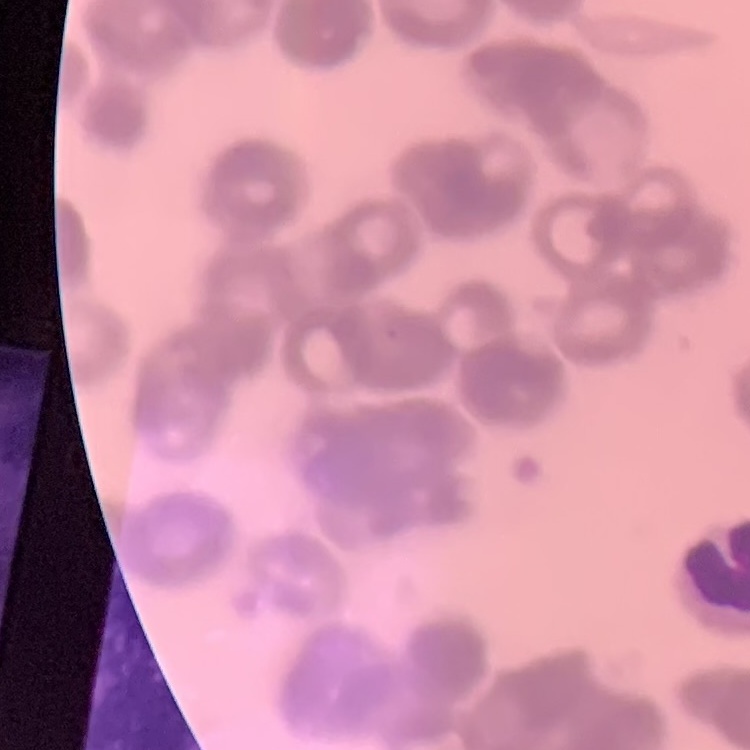
{
  "red_blood_cell_morphology": "rouleaux formation",
  "preparation": "thin blood smear",
  "stain": "Field's or Giemsa",
  "image_type": "one tile cut from a larger photomicrograph"
}